Report the malaria status of this cell.
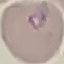
Parasitized.

capture = smartphone camera at the microscope eyepiece
image type = automatically extracted cell patch, resized to 64 × 64 pixels
preparation = thin blood film
stain = Giemsa